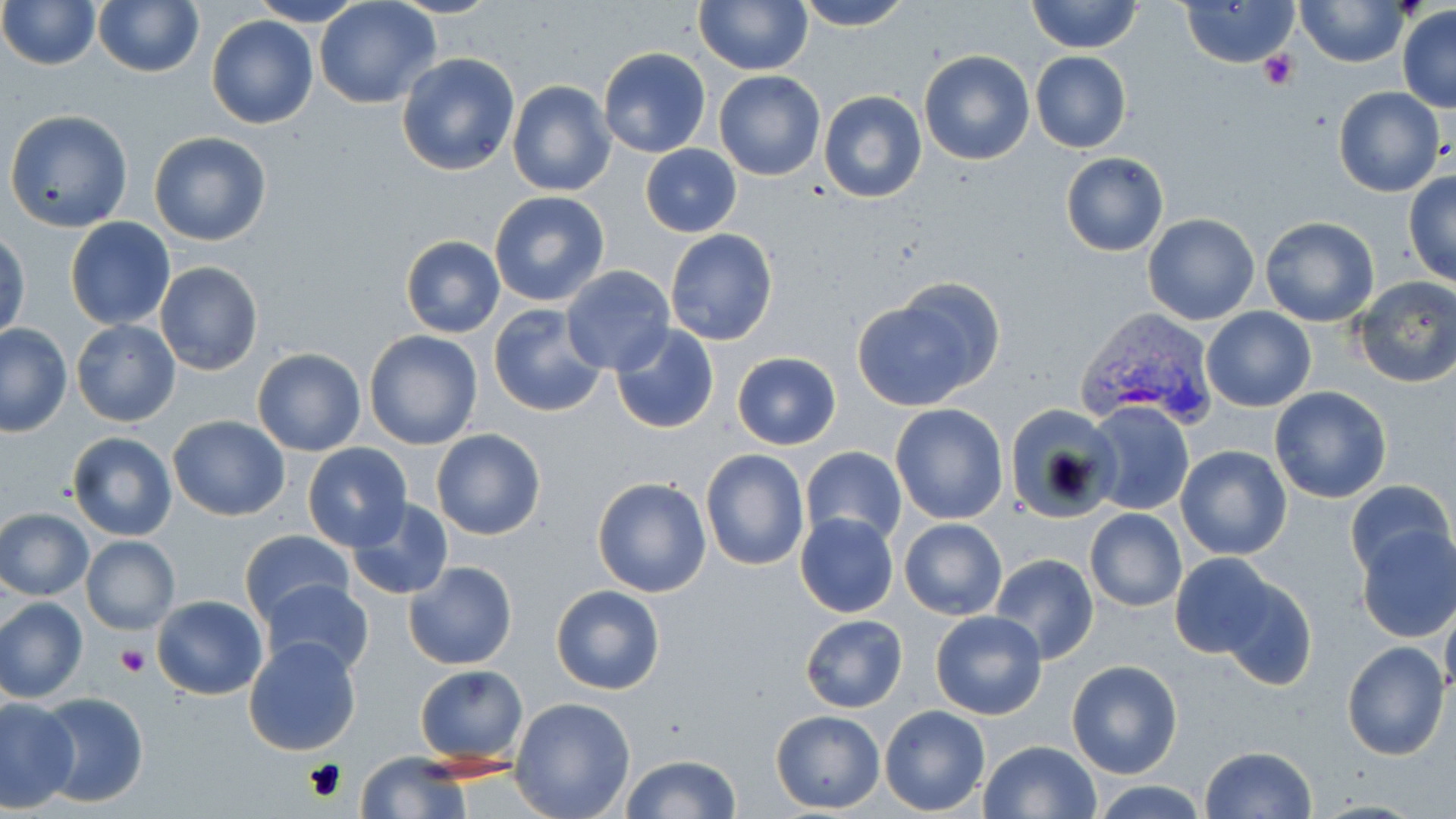
slide-level diagnosis = Plasmodium vivax
image size = 1456×819 pixels
Plasmodium vivax-infected red blood cell locations = approximate bounding boxes as (x1,y1)-(x2,y2) corner pairs in pixels: (1075,309)-(1218,429)
modality = light microscopy
field of view = single
preparation = thin blood film
magnification = 1000x
stain = May-Grünwald-Giemsa
uninfected red blood cell locations = approximate bounding boxes as (x1,y1)-(x2,y2) corner pairs in pixels: (0,0)-(100,70), (93,0)-(204,79), (248,0)-(366,26), (389,0)-(502,19), (693,0)-(813,75), (790,0)-(913,31), (1027,0)-(1142,54), (1180,0)-(1300,68), (1296,0)-(1409,68), (315,1)-(437,108), (1397,5)-(1456,111), (206,14)-(319,129), (598,46)-(711,159), (918,49)-(1033,165), (1030,51)-(1131,153), (396,52)-(521,176), (714,70)-(825,181), (507,80)-(616,197), (713,82)-(927,191), (1333,86)-(1443,196), (819,91)-(927,204), (4,108)-(134,233), (148,131)-(272,246), (640,143)-(742,237), (1061,153)-(1168,256), (1404,172)-(1456,286), (488,190)-(610,307), (1143,212)-(1260,325), (1259,215)-(1380,327), (64,217)-(176,330), (665,229)-(779,346), (1,230)-(29,340), (401,235)-(505,338), (154,261)-(265,377), (561,266)-(676,375), (1349,278)-(1456,388), (851,288)-(994,412), (487,304)-(608,418), (1201,307)-(1317,413), (71,320)-(181,426), (1,323)-(74,436), (610,323)-(719,435), (364,329)-(483,450), (252,348)-(366,457), (731,352)-(841,451), (1269,385)-(1393,503), (1005,401)-(1117,521), (1085,401)-(1194,517), (890,403)-(1009,525), (168,416)-(290,520), (431,428)-(546,540), (66,430)-(179,542), (302,442)-(413,553), (801,446)-(907,548), (1174,446)-(1292,562), (700,448)-(810,571), (590,476)-(712,598), (1345,479)-(1453,581), (346,498)-(454,602), (0,508)-(95,600), (1084,508)-(1187,613), (795,512)-(898,618), (899,518)-(1008,619), (1355,525)-(1456,644), (240,529)-(353,626), (81,536)-(180,635), (1169,551)-(1280,656), (989,554)-(1098,666), (403,560)-(518,670), (1218,576)-(1319,692), (259,578)-(373,677), (550,584)-(666,696), (152,594)-(269,700), (0,597)-(88,704), (1440,601)-(1456,701), (930,610)-(1048,721), (800,615)-(908,712), (243,636)-(362,756), (1340,641)-(1449,761), (1065,660)-(1182,779), (414,664)-(528,768), (35,693)-(151,807), (0,697)-(79,812), (510,697)-(637,819), (880,705)-(991,815), (771,709)-(884,813), (979,740)-(1101,819), (1199,746)-(1317,819), (356,754)-(468,819), (619,754)-(744,818), (1088,779)-(1210,818)
platelet locations = approximate bounding boxes as (x1,y1)-(x2,y2) corner pairs in pixels: (1259,49)-(1299,89), (116,643)-(147,675)